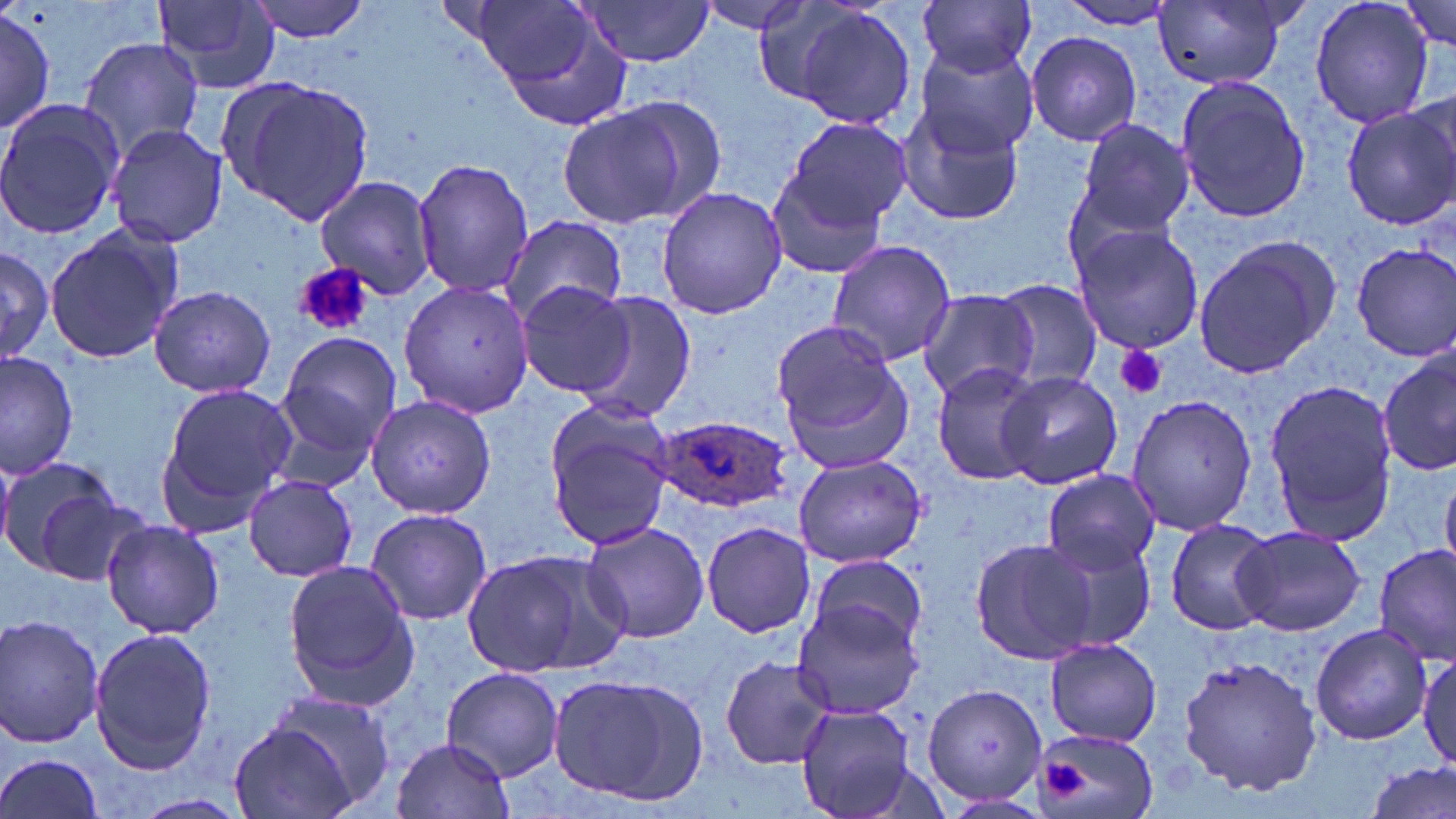

slide-level diagnosis = Plasmodium ovale
preparation = thin blood film
field of view = one of a larger specimen
platelet locations = approximate bounding boxes as (x1,y1)-(x2,y2) corner pairs in pixels: (297,265)-(372,336), (1116,344)-(1168,400), (1043,761)-(1090,801)
image size = 1456×819 pixels
modality = optical microscopy
uninfected red blood cell locations = approximate bounding boxes as (x1,y1)-(x2,y2) corner pairs in pixels: (245,0)-(373,44), (465,0)-(618,105), (575,0)-(715,67), (694,0)-(815,36), (749,0)-(872,104), (1310,0)-(1434,131), (1396,0)-(1452,51), (916,2)-(1039,81), (1051,2)-(1184,30), (151,3)-(282,93), (789,3)-(919,132), (1157,3)-(1292,90), (0,7)-(56,136), (1027,32)-(1141,146), (76,36)-(204,164), (913,44)-(1040,157), (1175,77)-(1311,224), (221,78)-(375,226), (0,97)-(124,243), (893,103)-(1024,227), (1337,103)-(1456,229), (555,105)-(695,226), (782,117)-(914,231), (1073,117)-(1195,239), (104,123)-(229,248), (412,157)-(533,298), (766,168)-(890,279), (312,175)-(438,301), (655,186)-(786,319), (494,215)-(626,330), (1068,223)-(1205,356), (42,224)-(185,366), (1191,239)-(1337,380), (827,240)-(956,367), (0,243)-(54,366), (1351,243)-(1455,360), (398,277)-(535,418), (988,279)-(1101,392), (515,280)-(634,396), (147,285)-(277,397), (573,289)-(697,423), (916,289)-(1036,401), (773,319)-(911,472), (274,331)-(403,462), (1379,348)-(1456,480), (1,351)-(79,481), (931,362)-(1048,486), (996,371)-(1123,490), (1264,378)-(1397,546), (154,382)-(297,532), (364,393)-(496,520), (1125,393)-(1257,537), (541,398)-(675,553), (0,453)-(122,576), (794,454)-(926,568), (1040,469)-(1160,574), (243,475)-(360,581), (1442,475)-(1456,570), (365,507)-(492,627), (101,518)-(225,640), (1165,518)-(1279,636), (579,520)-(710,644), (700,520)-(814,639), (1233,524)-(1365,636), (1041,532)-(1160,652), (966,536)-(1103,666), (1375,545)-(1454,665), (461,549)-(626,678), (807,555)-(930,654), (283,563)-(418,709), (794,600)-(922,719), (0,614)-(105,751), (1310,624)-(1430,744), (87,626)-(217,775), (1045,638)-(1162,746), (1412,647)-(1456,770), (719,653)-(834,769), (1176,654)-(1323,797), (441,666)-(563,780), (546,669)-(711,808), (923,683)-(1050,806), (264,688)-(394,811), (794,703)-(915,819), (226,719)-(366,819), (1030,728)-(1161,819), (391,735)-(514,818), (0,752)-(105,818), (1364,762)-(1454,819), (134,792)-(248,817)
magnification = 1000x
Plasmodium ovale-infected red blood cell locations = approximate bounding boxes as (x1,y1)-(x2,y2) corner pairs in pixels: (650,411)-(797,514)
stain = May-Grünwald-Giemsa